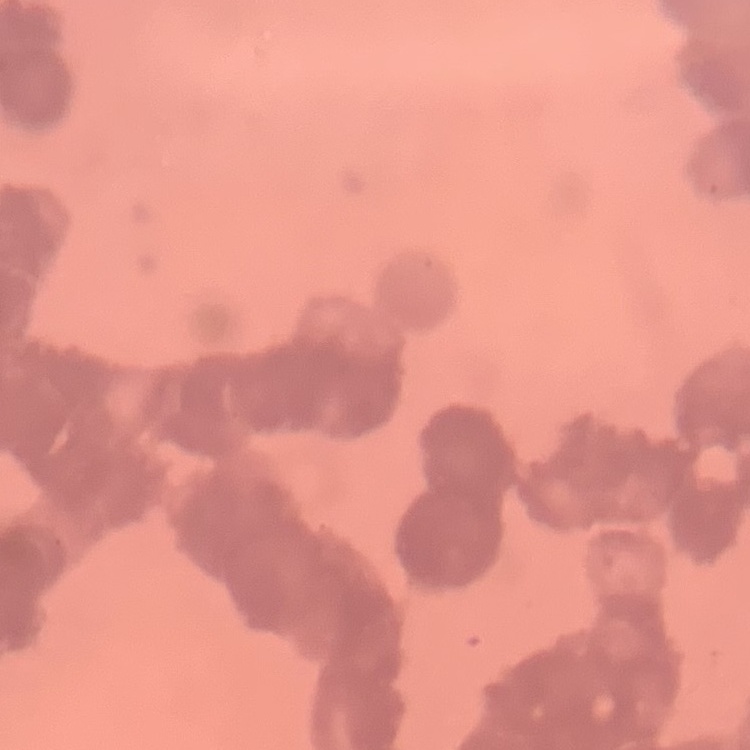
The erythrocytes show rouleaux formation. Square crop of a larger photomicrograph. Field's or Giemsa stain. Thin peripheral smear.